Report the malaria status of this cell.
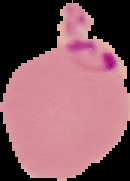
Parasitized.

From a thin blood film. The area outside the segmented cell region is set to black. Image is 130×181 pixels.